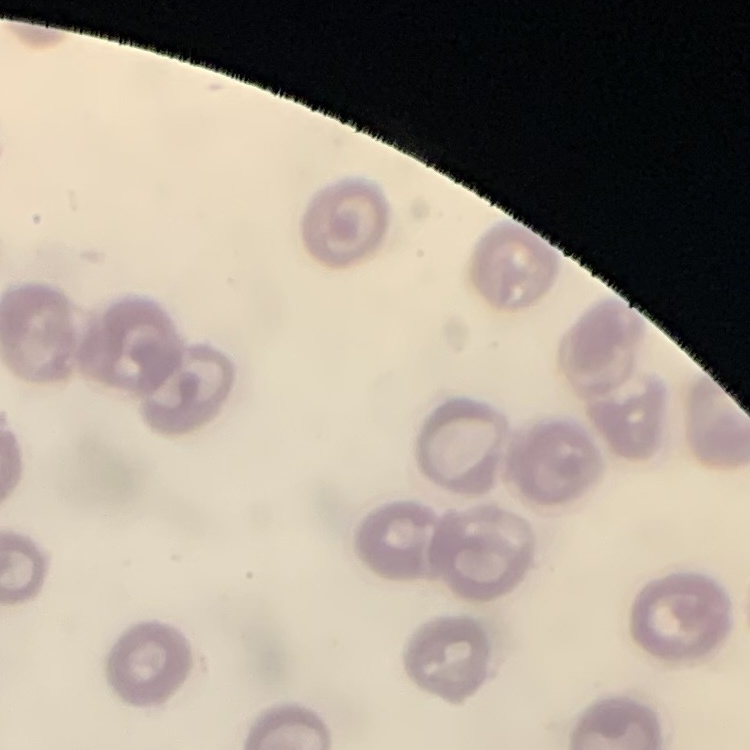

red blood cell morphology = no rouleaux formation
stain = Field's or Giemsa
preparation = thin blood smear
image type = square crop of a larger photomicrograph